Comment on the morphology of the erythrocytes.
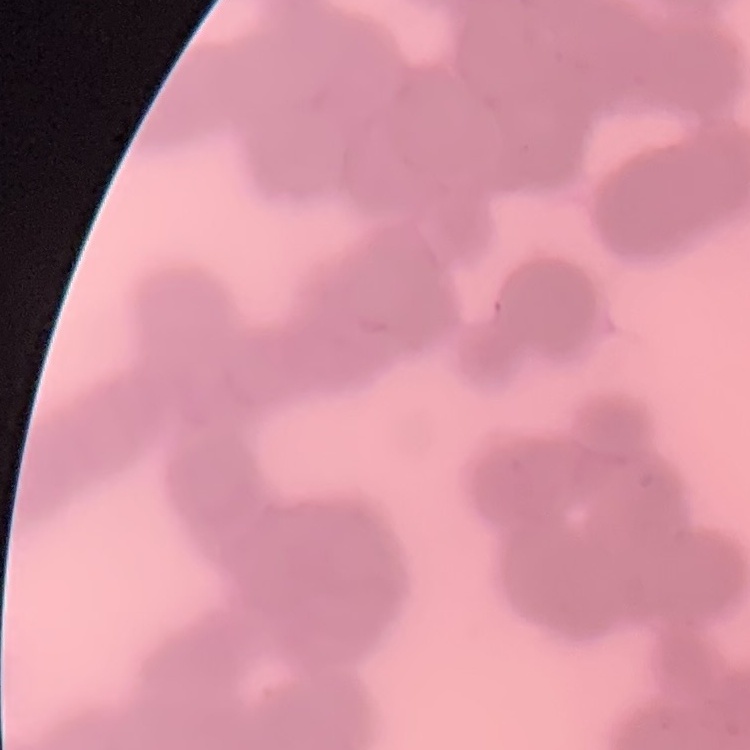
They show rouleaux formation.

Summary:
  - Image type: square crop of a larger photomicrograph
  - Preparation: thin blood smear
  - Stain: Field's or Giemsa